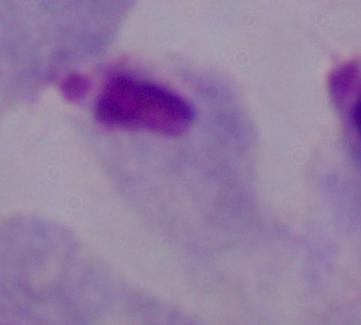
Micrograph. Captured at 1000x magnification. A trichomonad is seen.